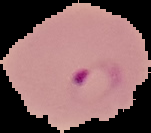
{
  "preparation": "thin blood film",
  "image_size": "151×133 pixels",
  "image_type": "cell region segmented out of the field of view; surrounding area masked to black",
  "result": "Plasmodium parasites detected"
}